Assess the morphology of the red blood cells.
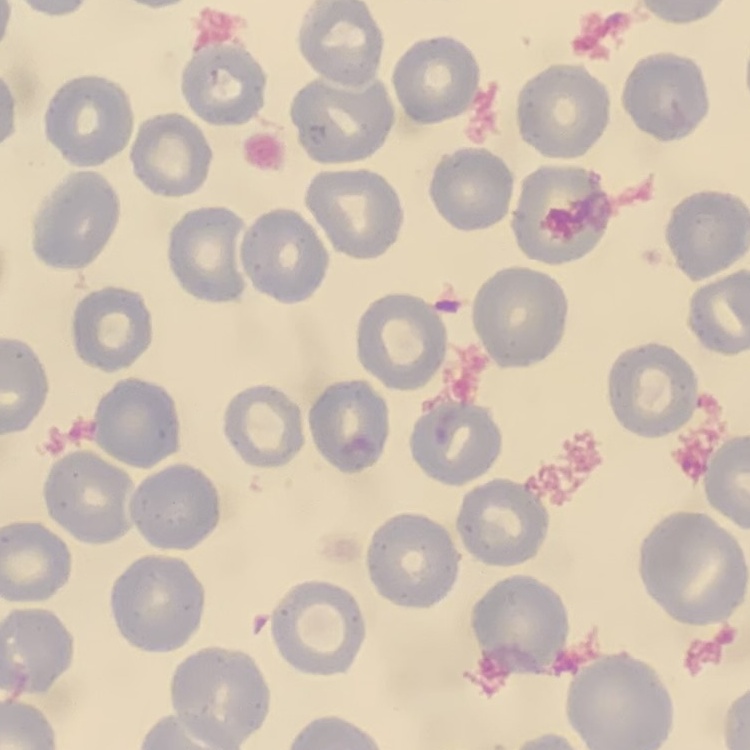
No rouleaux formation.

preparation = thin peripheral smear
stain = Field's or Giemsa
image type = square crop of a larger photomicrograph